Report the malaria status of this cell.
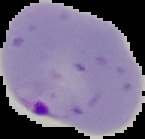
Parasitized.

Summary:
  - Image size: 145×139 pixels
  - Preparation: thin blood smear
  - Image type: segmented cell region on a black background